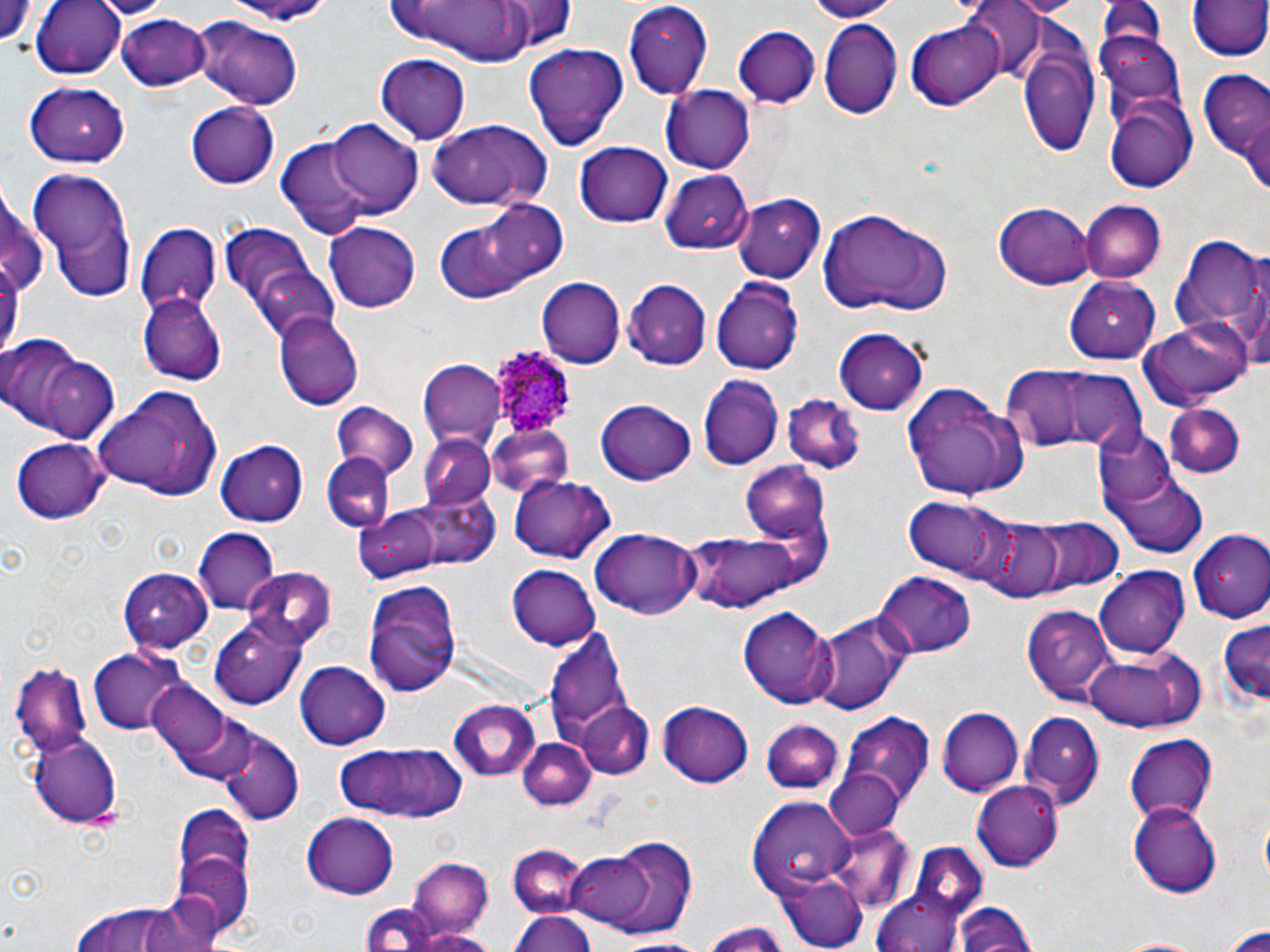

slide-level diagnosis = Plasmodium ovale
preparation = thin blood smear
magnification = 1000x
uninfected red blood cell locations = approximate bounding boxes as [x1, y1, x2, y2] in pixels: [31, 0, 128, 78], [96, 0, 172, 18], [212, 0, 343, 23], [496, 0, 575, 50], [806, 0, 903, 20], [965, 0, 1045, 79], [1096, 0, 1170, 47], [1186, 0, 1269, 63], [0, 2, 41, 46], [384, 2, 548, 61], [622, 2, 716, 103], [118, 14, 210, 91], [189, 15, 304, 110], [905, 16, 1006, 109], [818, 20, 903, 119], [734, 27, 820, 107], [1015, 40, 1101, 158], [524, 42, 628, 152], [376, 53, 470, 143], [1198, 73, 1270, 160], [25, 82, 133, 167], [661, 86, 756, 174], [1104, 90, 1197, 192], [185, 101, 279, 189], [1237, 109, 1270, 196], [328, 119, 422, 215], [427, 119, 553, 213], [277, 136, 375, 239], [575, 141, 673, 227], [656, 168, 755, 258], [30, 170, 136, 302], [733, 196, 825, 282], [452, 198, 572, 294], [993, 199, 1094, 288], [1079, 201, 1164, 284], [816, 205, 953, 317], [134, 222, 224, 310], [323, 222, 421, 312], [1168, 235, 1269, 351], [227, 238, 339, 345], [1065, 275, 1163, 364], [538, 277, 625, 367], [711, 277, 805, 374], [624, 279, 711, 367], [139, 294, 227, 382], [273, 313, 364, 409], [1141, 320, 1254, 407], [835, 328, 929, 411], [0, 337, 107, 442], [423, 359, 504, 446], [1001, 366, 1099, 449], [1048, 369, 1148, 452], [697, 377, 782, 471], [901, 382, 1029, 499], [93, 386, 219, 497], [787, 392, 862, 472], [597, 399, 696, 485], [1163, 402, 1243, 478], [331, 403, 420, 478], [486, 425, 575, 503], [1092, 426, 1178, 512], [420, 436, 494, 509], [11, 439, 111, 525], [215, 439, 308, 526], [319, 453, 393, 533], [740, 461, 833, 542], [1111, 469, 1208, 555], [511, 476, 614, 564], [408, 489, 501, 569], [900, 496, 1013, 578], [354, 507, 441, 585], [1025, 516, 1121, 595], [971, 517, 1077, 602], [191, 527, 280, 612], [590, 529, 701, 621], [680, 529, 809, 612], [1188, 532, 1270, 624], [508, 564, 601, 651], [119, 566, 212, 650], [1095, 567, 1192, 657], [245, 568, 337, 652], [875, 572, 975, 659], [362, 578, 468, 696], [1023, 603, 1118, 705], [737, 606, 836, 708], [809, 607, 914, 717], [211, 615, 305, 708], [1216, 619, 1270, 709], [541, 625, 640, 761], [87, 648, 186, 733], [1080, 648, 1205, 733], [296, 661, 391, 747], [10, 662, 95, 759], [148, 683, 234, 764], [449, 700, 541, 783], [576, 701, 655, 780], [658, 702, 753, 787], [936, 706, 1024, 797], [837, 712, 935, 816], [1020, 712, 1104, 810], [761, 720, 843, 794], [217, 726, 305, 825], [27, 733, 121, 825], [1125, 735, 1216, 821], [518, 738, 594, 810], [329, 739, 467, 824], [824, 767, 905, 840], [974, 781, 1064, 869], [749, 798, 853, 898], [1131, 801, 1225, 894], [172, 809, 255, 931], [301, 813, 399, 901], [828, 820, 913, 908], [564, 835, 696, 940], [507, 845, 592, 919], [408, 858, 494, 940], [773, 872, 866, 950], [870, 878, 973, 951], [138, 896, 223, 952], [73, 903, 187, 952], [951, 903, 1038, 952], [360, 906, 447, 951], [507, 909, 597, 952], [698, 923, 796, 951], [1222, 924, 1270, 951], [412, 928, 504, 952], [609, 935, 718, 950]
stain = May-Grünwald-Giemsa
field of view = single
Plasmodium ovale-infected red blood cell locations = approximate bounding boxes as [x1, y1, x2, y2] in pixels: [488, 345, 576, 437]
image size = 1270×952 pixels
modality = light microscopy